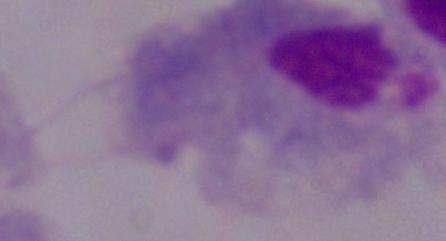

Summary:
  - Modality: photomicrograph
  - Identification: trichomonad
  - Magnification: 1000x